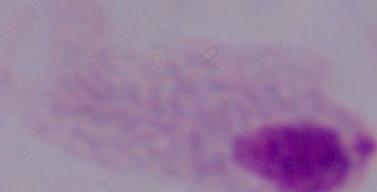
{
  "identification": "trichomonad",
  "magnification": "1000x",
  "modality": "micrograph"
}